Locate every P. falciparum parasite and give its life-cycle stage, and locate every leukocyte and any debris.
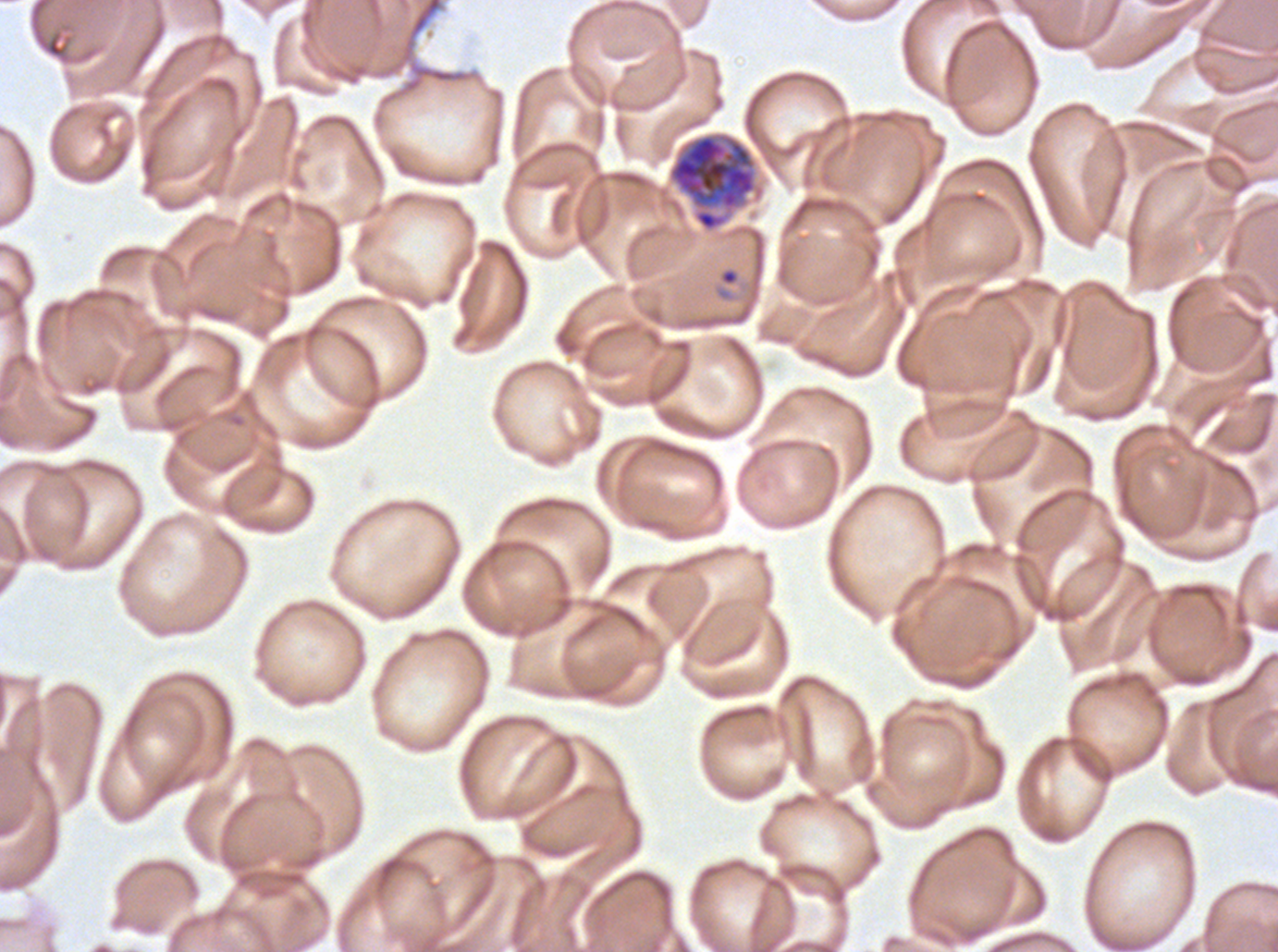

Approximate bounding boxes as {x1, y1, x2, y2} in pixels.
Rings: {721, 270, 737, 285}.
Early schizonts: {667, 131, 764, 233}.
No late-ring/early-trophozoite forms, mid trophozoites, late trophozoites, late schizonts, segmenters, gametocytes, leukocytes, or debris observed.

specimen = P. falciparum cultured ex vivo for 24 to 48 hours, from a patient in The Gambia
life-cycle stages observed = ring, early schizont
preparation = thin blood smear
stain = Giemsa
field of view = one sub-image of a larger composite
image size = 1278×952 pixels